Name the parasite shown.
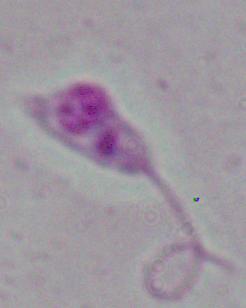

Leishmania.

Summary:
  - Magnification: 1000x
  - Modality: micrograph